Find the cells and give the type of each one.
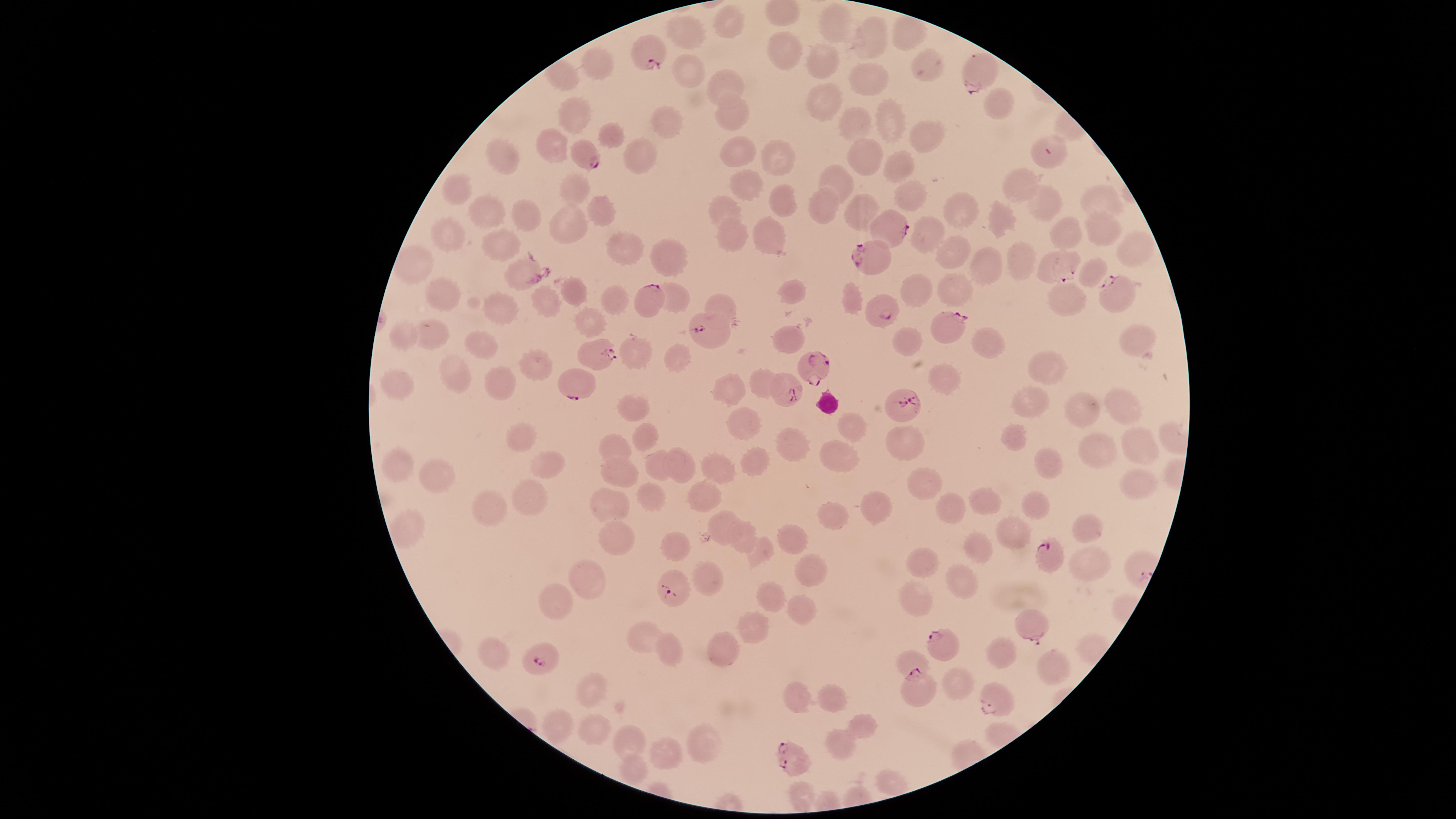

Approximate marker points as (x, y) in pixels.
Parasitized red blood cells: (647, 54), (983, 74), (585, 150), (1043, 154), (890, 222), (876, 256), (1063, 266), (1118, 293), (651, 302), (879, 307), (946, 329), (713, 334), (596, 351), (813, 364), (576, 385), (786, 386), (901, 402), (1049, 556), (674, 587), (1033, 628), (940, 643), (542, 660), (925, 688), (995, 698), (793, 757).
Uninfected red blood cells: (726, 21), (838, 25), (687, 31), (879, 36), (784, 54), (826, 61), (929, 66), (601, 67), (685, 69), (866, 74), (969, 75), (722, 81), (822, 101), (998, 103), (576, 113), (671, 113), (732, 116), (851, 120), (887, 123), (922, 133), (615, 136), (556, 145), (742, 152), (503, 156), (643, 156), (775, 156), (870, 156), (898, 159), (840, 180), (751, 184), (1014, 187), (457, 188), (577, 188), (909, 193), (781, 196), (1104, 198), (1045, 203), (724, 204), (601, 206), (825, 206), (487, 211), (522, 212), (863, 212), (996, 217), (964, 218), (563, 224), (1101, 229), (926, 231), (449, 233), (771, 233), (1070, 234), (733, 236), (503, 241), (626, 245), (1139, 245), (1023, 250), (673, 256), (958, 257), (516, 269), (997, 269), (920, 289), (444, 290), (958, 290), (791, 292), (575, 293), (617, 293), (678, 294), (1069, 297), (550, 301), (852, 302), (723, 306), (506, 307), (592, 317), (410, 333), (436, 336), (790, 336), (904, 339), (1141, 340), (994, 346), (481, 347), (630, 348), (670, 355), (537, 363), (455, 368), (1039, 368), (499, 379), (951, 382), (404, 383), (736, 383), (764, 383), (1029, 401), (639, 406), (1081, 408), (1121, 409), (854, 422), (747, 425), (1013, 434), (649, 437), (903, 437), (518, 440), (794, 441), (1098, 444), (619, 446), (841, 449), (1136, 450), (756, 455), (660, 462), (408, 464), (687, 466), (1046, 466), (551, 467), (722, 467), (622, 473), (445, 477), (919, 477), (1133, 484), (653, 497), (989, 497), (528, 498), (873, 499), (699, 500), (609, 501), (496, 502), (1041, 503), (949, 507), (728, 515), (836, 515), (1089, 526), (414, 527), (1019, 533), (746, 534), (612, 538), (787, 539), (974, 543), (678, 546), (761, 550), (1098, 563), (924, 565), (814, 569), (712, 572), (588, 578), (963, 579), (915, 596), (562, 598), (768, 598), (803, 608), (751, 624), (645, 632), (733, 645), (1000, 648), (492, 651), (675, 652), (909, 660), (1052, 666), (960, 681), (593, 691), (800, 691), (835, 697), (863, 724), (558, 726), (601, 728), (844, 737), (629, 738), (706, 739), (664, 752), (633, 766).
No white blood cells identified.

{
  "visible_region": "circular",
  "field_of_view": "single",
  "capture": "smartphone photograph through the microscope eyepiece",
  "image_size": "1456×819 pixels",
  "stain": "Giemsa",
  "preparation": "thin blood smear",
  "species": "Plasmodium falciparum"
}